Give the preparation type.
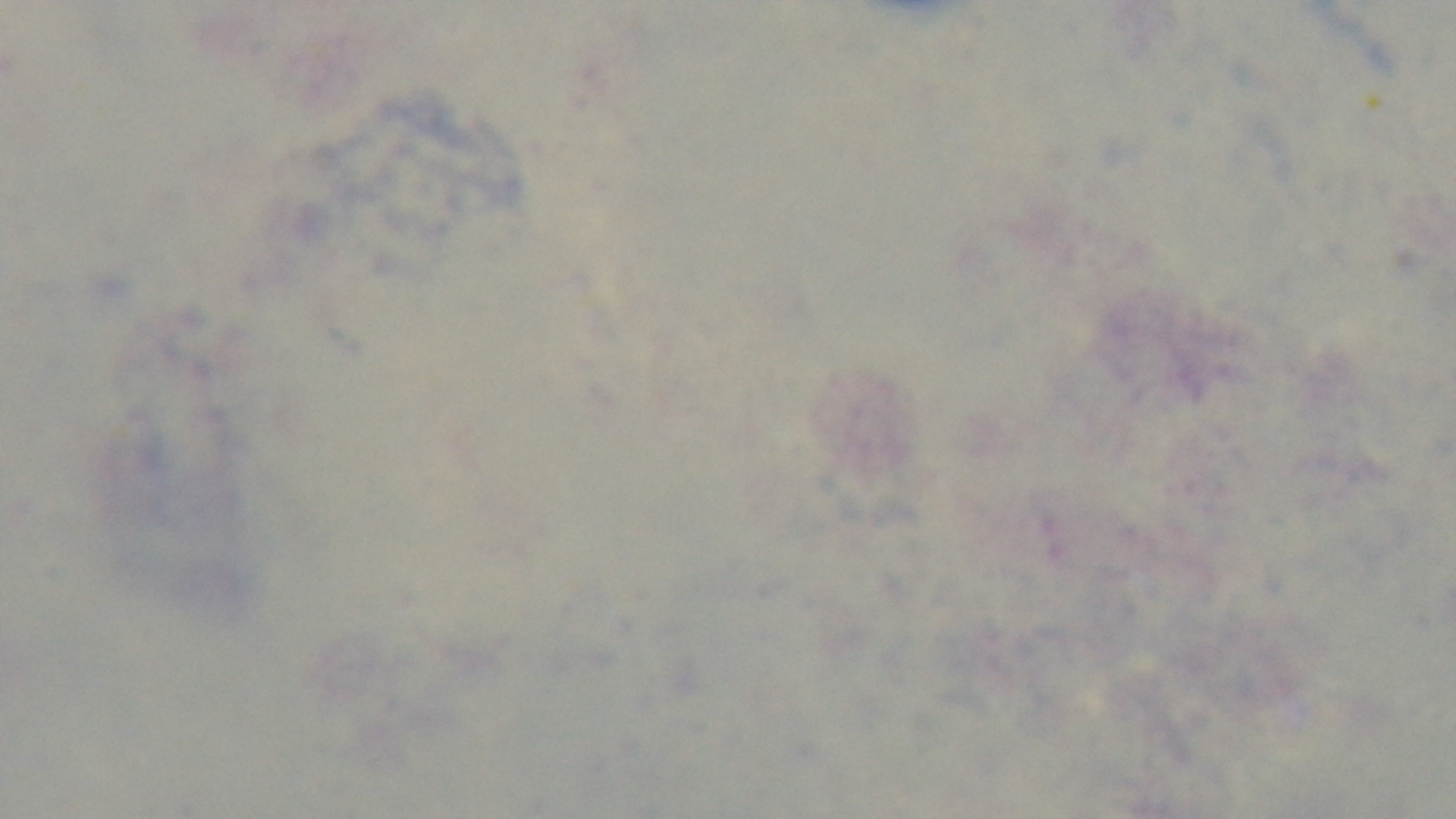
A thick smear.

Malaria status: uninfected. Giemsa stain. Light microscopy. Oil-immersion objective, 100x. Single field of view. Captured with a mounted 4K digital camera.